Give the position of every Plasmodium parasite visible.
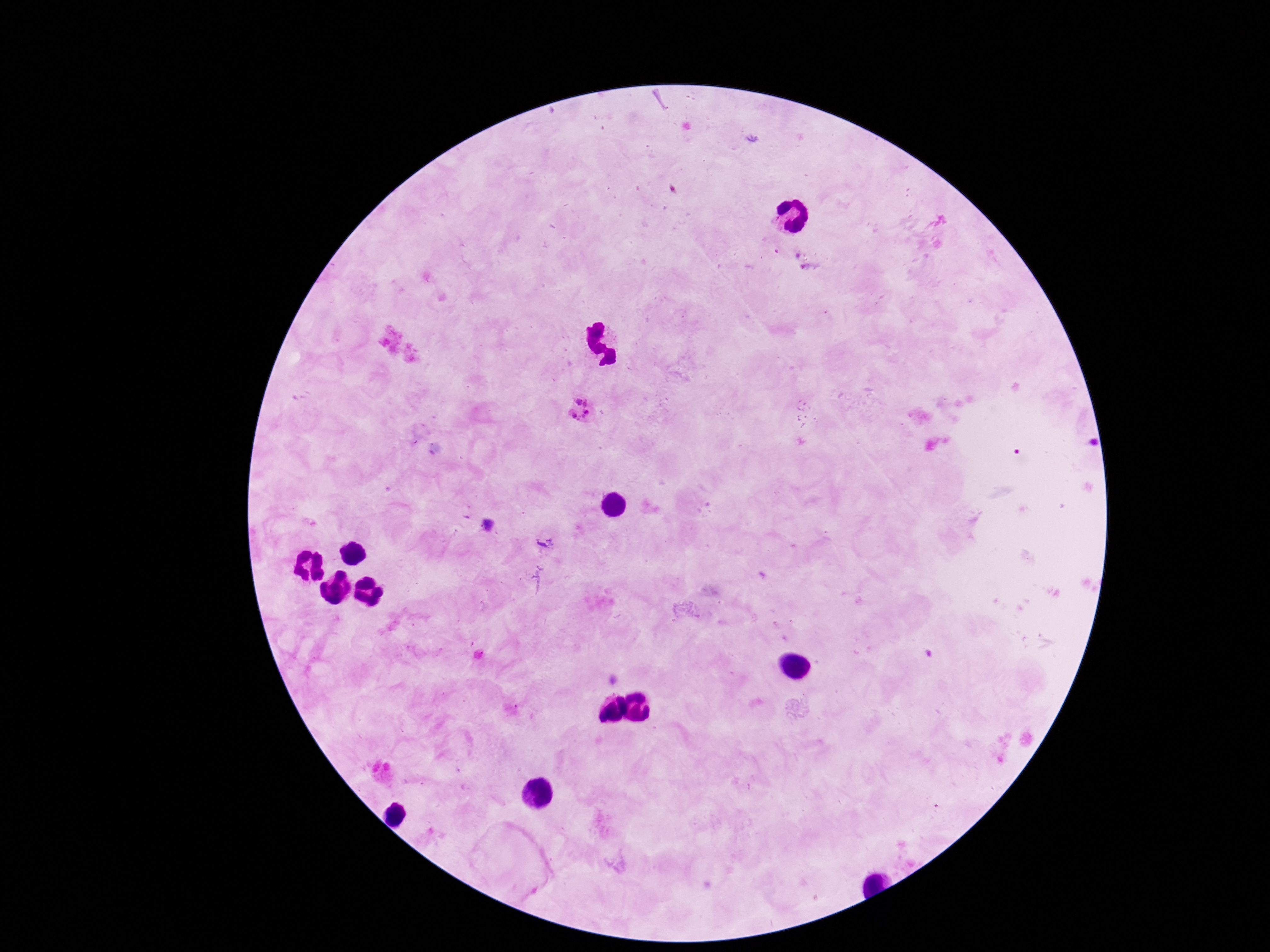

Approximate object centers, in pixels from the top-left corner.
Plasmodium parasites: (x=798, y=252), (x=810, y=271), (x=584, y=412), (x=545, y=541).

Summary:
  - Patient malaria status: infected
  - Magnification: 100x
  - Image size: 1270×952 pixels
  - Stain: Giemsa
  - Capture: smartphone camera through the microscope eyepiece
  - Field of view: one from this slide
  - Preparation: thick blood smear